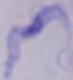
identification = trypanosome
magnification = 1000x
modality = micrograph